Locate every uninfected red blood cell.
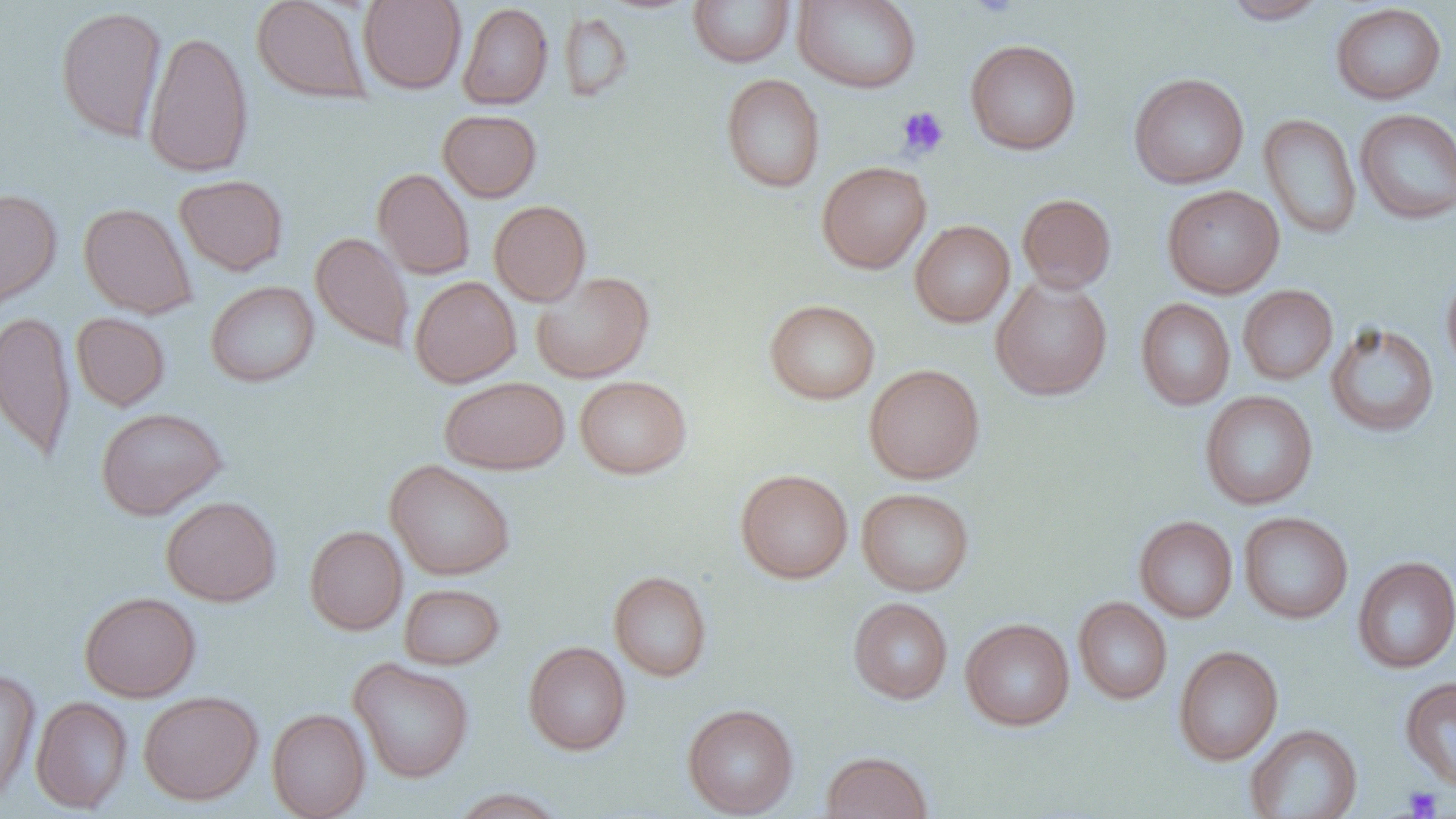

Approximate bounding boxes as [x1, y1, x2, y2] in pixels.
Uninfected red blood cells: [251, 0, 370, 103], [358, 0, 466, 94], [688, 0, 796, 67], [1220, 0, 1329, 24], [793, 1, 921, 93], [1331, 2, 1447, 104], [457, 3, 553, 109], [55, 5, 168, 142], [559, 11, 634, 102], [143, 30, 254, 177], [965, 39, 1081, 155], [721, 73, 825, 193], [1129, 73, 1249, 188], [438, 109, 542, 201], [1355, 109, 1456, 224], [1259, 113, 1361, 239], [817, 161, 931, 273], [372, 168, 475, 280], [174, 174, 289, 275], [1162, 185, 1284, 298], [0, 187, 62, 312], [1017, 193, 1117, 293], [489, 200, 591, 306], [78, 202, 196, 319], [910, 220, 1015, 327], [311, 231, 414, 354], [1441, 267, 1456, 380], [531, 270, 655, 384], [410, 275, 521, 388], [990, 276, 1113, 400], [205, 280, 319, 387], [1238, 285, 1338, 385], [1135, 298, 1235, 410], [764, 299, 880, 404], [0, 310, 76, 462], [71, 312, 170, 411], [1325, 322, 1440, 438], [864, 364, 985, 484], [574, 375, 691, 479], [439, 376, 570, 474], [1200, 390, 1318, 510], [95, 406, 227, 519], [385, 460, 516, 580], [736, 469, 853, 583], [856, 487, 974, 596], [161, 496, 281, 606], [1239, 511, 1353, 624], [1134, 515, 1238, 623], [304, 525, 408, 635], [1352, 556, 1456, 674], [608, 570, 712, 682], [399, 583, 504, 670], [79, 591, 201, 702], [1073, 597, 1173, 704], [848, 598, 953, 704], [960, 618, 1075, 731], [523, 641, 631, 755], [1173, 645, 1284, 765], [349, 658, 474, 783], [0, 667, 41, 804], [1400, 676, 1456, 792], [138, 690, 263, 805], [31, 696, 133, 814], [682, 703, 799, 818], [267, 708, 371, 819], [1245, 724, 1362, 818], [820, 751, 933, 819], [448, 787, 568, 818].

Platelet locations: [969, 0, 1021, 19], [896, 105, 949, 159], [1402, 785, 1443, 818]. Slide-level diagnosis: no evidence of blood parasites. 1000x magnification. Light microscopy. Image is 1456×819 pixels. Single field of view. Thin blood smear.